Outline each blood parasite and name the species.
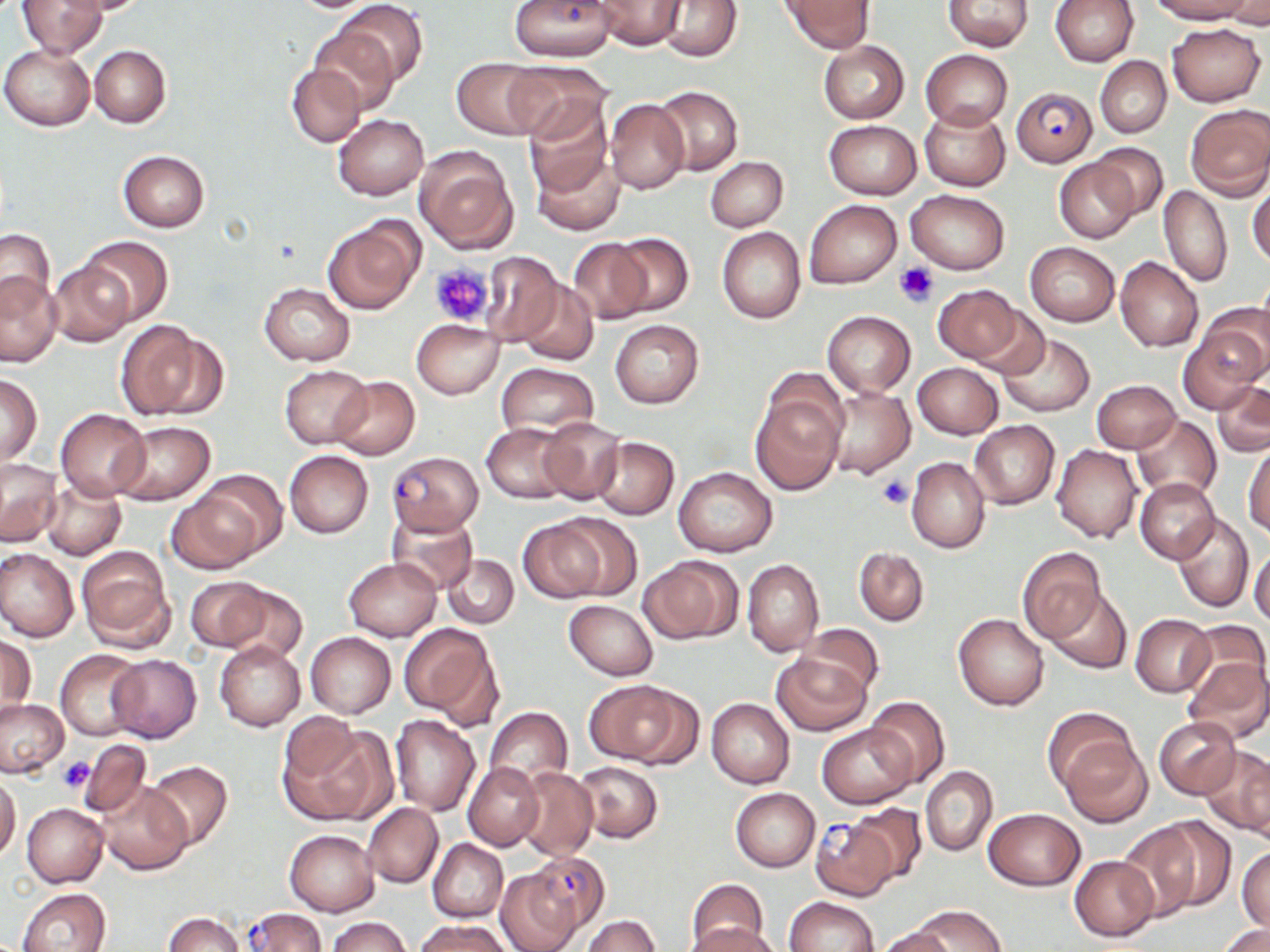
Approximate bounding boxes as (x1,y1)-(x2,y2) corner pairs in pixels.
Plasmodium falciparum-infected red blood cells: (507,0)-(616,61), (1011,87)-(1097,167), (387,450)-(483,534), (810,815)-(900,901), (523,850)-(611,938), (241,907)-(326,952).
No Plasmodium ovale, Plasmodium malariae, Plasmodium vivax, Babesia divergens, or Trypanosoma brucei observed.

Summary:
  - Uninfected red blood cell locations: (17,0)-(107,57), (64,0)-(154,15), (657,0)-(743,62), (780,0)-(875,51), (1051,0)-(1139,66), (1148,0)-(1255,24), (335,1)-(428,87), (593,1)-(688,49), (943,1)-(1035,51), (1220,1)-(1270,29), (308,23)-(400,115), (1166,23)-(1266,107), (818,41)-(910,124), (1,44)-(96,131), (89,45)-(171,128), (921,50)-(1012,129), (1095,56)-(1171,136), (452,58)-(546,138), (501,62)-(609,142), (287,63)-(366,148), (653,85)-(742,176), (525,96)-(614,198), (605,99)-(689,194), (1184,103)-(1270,199), (919,105)-(1010,190), (333,114)-(427,200), (824,120)-(921,198), (1088,142)-(1168,218), (413,145)-(518,255), (531,148)-(625,236), (118,149)-(209,232), (705,156)-(788,231), (1055,158)-(1140,243), (1249,178)-(1270,269), (1159,185)-(1232,287), (905,188)-(1011,274), (805,200)-(901,288), (322,215)-(424,314), (717,227)-(806,324), (0,229)-(56,311), (607,232)-(694,317), (78,236)-(173,326), (566,238)-(652,324), (1025,242)-(1120,326), (479,251)-(563,346), (1116,257)-(1203,352), (46,262)-(133,347), (0,273)-(62,365), (517,279)-(598,365), (259,283)-(354,365), (932,284)-(1025,364), (1204,302)-(1270,384), (973,305)-(1049,381), (822,310)-(915,398), (411,319)-(505,399), (610,319)-(703,408), (1181,320)-(1265,412), (115,321)-(214,420), (996,333)-(1096,419), (495,363)-(598,440), (912,363)-(1003,439), (279,364)-(372,448), (0,374)-(41,465), (329,375)-(421,460), (1091,379)-(1181,453), (1212,379)-(1270,458), (823,385)-(913,479), (751,393)-(843,494), (56,408)-(150,500), (1133,415)-(1221,500), (538,417)-(624,503), (969,420)-(1058,509), (112,421)-(216,506), (482,423)-(575,503), (593,437)-(678,519), (1245,437)-(1270,538), (1051,444)-(1142,543), (284,450)-(374,538), (906,456)-(990,554), (0,458)-(63,547), (673,466)-(778,557), (40,478)-(125,561), (1136,479)-(1219,562), (168,484)-(272,574), (386,510)-(479,595), (1172,513)-(1255,612), (517,518)-(613,603), (76,546)-(175,651), (854,547)-(929,627), (1249,547)-(1270,628), (1018,548)-(1105,641), (0,549)-(79,643), (443,555)-(518,628), (345,557)-(440,642), (639,557)-(741,644), (742,558)-(824,657), (186,577)-(271,651), (219,582)-(307,663), (1045,588)-(1132,675), (563,599)-(659,680), (953,613)-(1050,711), (1131,614)-(1215,697), (1181,620)-(1268,703), (399,621)-(501,725), (796,622)-(883,700), (306,632)-(396,718), (2,635)-(36,716), (214,642)-(305,731), (55,649)-(147,740), (772,652)-(872,736), (107,655)-(202,742), (1183,656)-(1270,743), (587,679)-(694,767), (707,697)-(794,788), (864,697)-(950,787), (0,698)-(67,777), (485,706)-(572,788), (1042,708)-(1138,799), (390,715)-(481,817), (1153,716)-(1241,799), (281,717)-(387,825), (818,723)-(917,809), (1057,737)-(1151,827), (80,738)-(151,819), (1199,748)-(1270,838), (145,760)-(234,850), (463,761)-(544,850), (574,761)-(662,842), (516,766)-(597,860), (922,766)-(997,856), (0,774)-(20,862), (97,781)-(191,875), (730,788)-(820,871), (362,803)-(443,888), (22,804)-(107,887), (844,804)-(928,885), (983,808)-(1086,890), (1147,816)-(1236,911), (1114,820)-(1207,922), (284,829)-(380,916), (428,839)-(508,922), (1237,846)-(1270,931), (1069,855)-(1160,942), (495,868)-(581,952), (686,880)-(769,950), (18,887)-(112,952), (785,897)-(880,951), (911,905)-(1007,952), (163,912)-(243,952), (583,916)-(660,952), (327,917)-(411,952), (417,919)-(513,952), (690,924)-(782,952), (1219,924)-(1270,952), (875,927)-(955,952)
  - Platelet locations: (429,262)-(495,327), (896,262)-(939,305), (877,475)-(912,510), (57,756)-(94,794)
  - Slide-level diagnosis: Plasmodium falciparum
  - Stain: May-Grünwald-Giemsa
  - Preparation: thin blood film
  - Image size: 1270×952 pixels
  - Magnification: 1000x
  - Field of view: one of a larger specimen
  - Modality: light microscopy